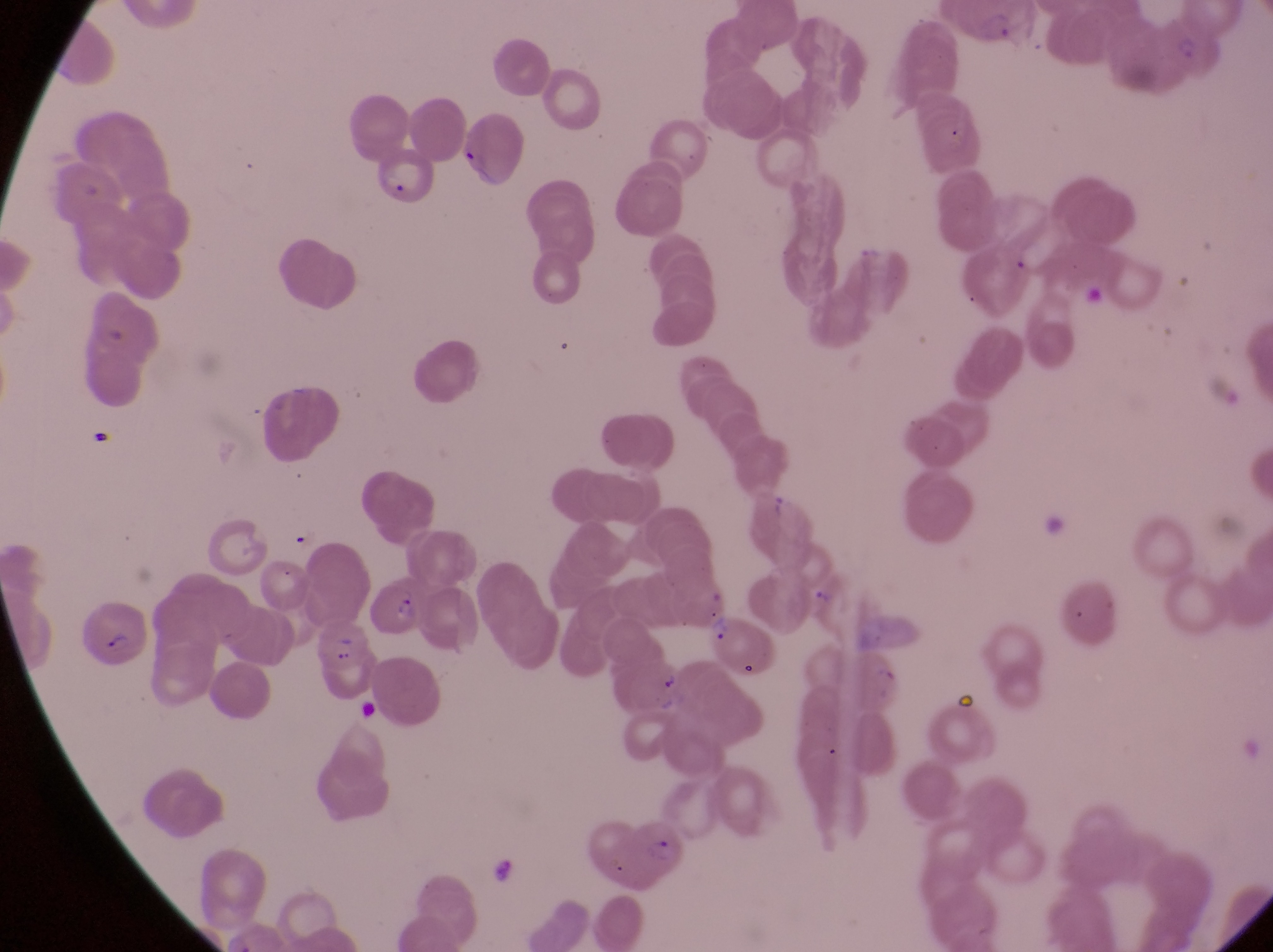

Approximate bounding boxes as [left, top, right, bottom] in pixels. Parasitised red blood cell locations: [451, 120, 528, 195], [374, 153, 439, 215], [365, 577, 427, 642], [78, 597, 143, 667], [702, 607, 772, 684], [312, 624, 374, 702], [629, 812, 689, 879]. Artifact (platelet-like body, stain precipitate, or debris) locations: [953, 691, 981, 723]. Image is 1273×952 pixels. Thin blood film. Magnification of 1000x. Photographed through the eyepiece of an Olympus CX-23 microscope with a smartphone camera. One field of view. Collected in Uganda.